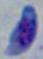

Summary:
  - Modality: micrograph
  - Identification: Toxoplasma gondii
  - Magnification: 1000x